Classify this cell by malaria status.
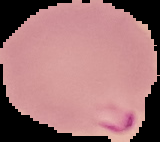

It is parasitized.

preparation = thin blood film
image size = 160×142 pixels
image type = cell region segmented out of the field of view; surrounding area masked to black